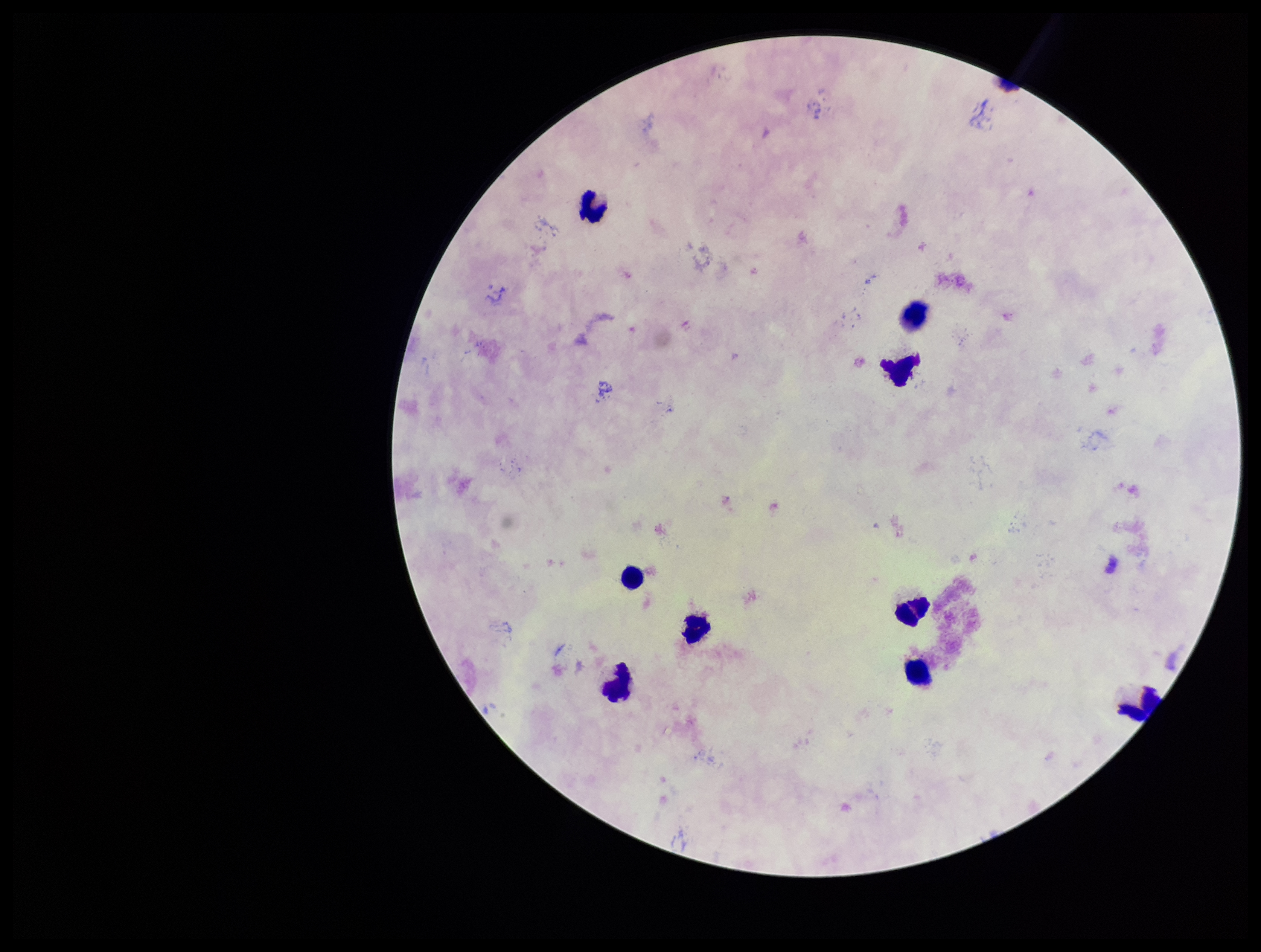

parasite count = 0
stain = Giemsa
image size = 1261×952 pixels
capture = smartphone photograph through the microscope eyepiece
preparation = thick blood smear
Plasmodium parasites = none seen
leukocyte count = 9
field of view = single
patient malaria status = negative